Classify this cell by malaria status.
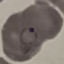

It is parasitized.

capture: smartphone through the microscope eyepiece
stain: Giemsa
image_type: automatically extracted cell patch, resized to 64 × 64 pixels
preparation: thin smear